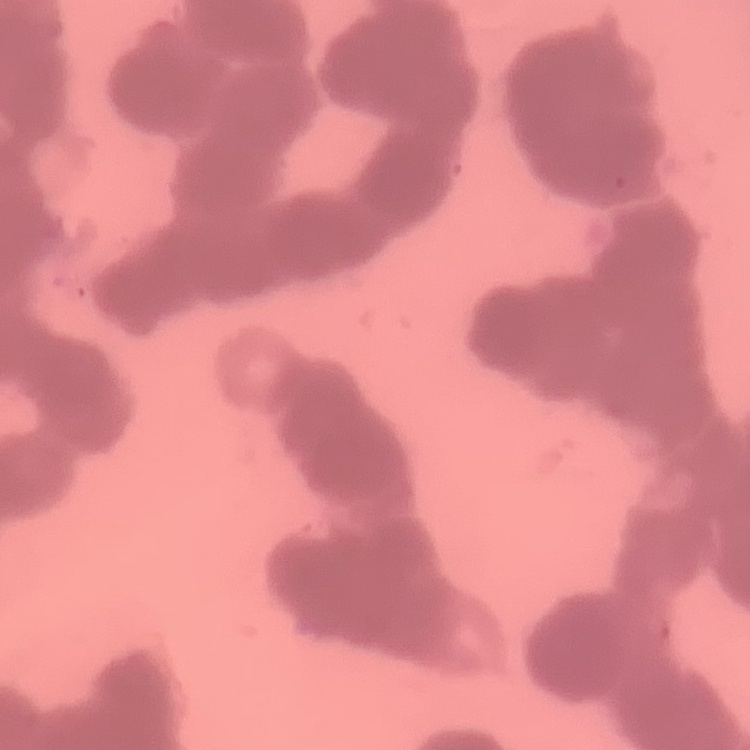

Summary:
  - Red blood cell morphology: rouleaux formation
  - Image type: one tile cut from a larger photomicrograph
  - Stain: Field's or Giemsa
  - Preparation: thin peripheral smear